Report the malaria status of this cell.
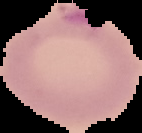
Uninfected.

Segmented cell region on a black background. From a thin blood film. Image is 142×133 pixels.